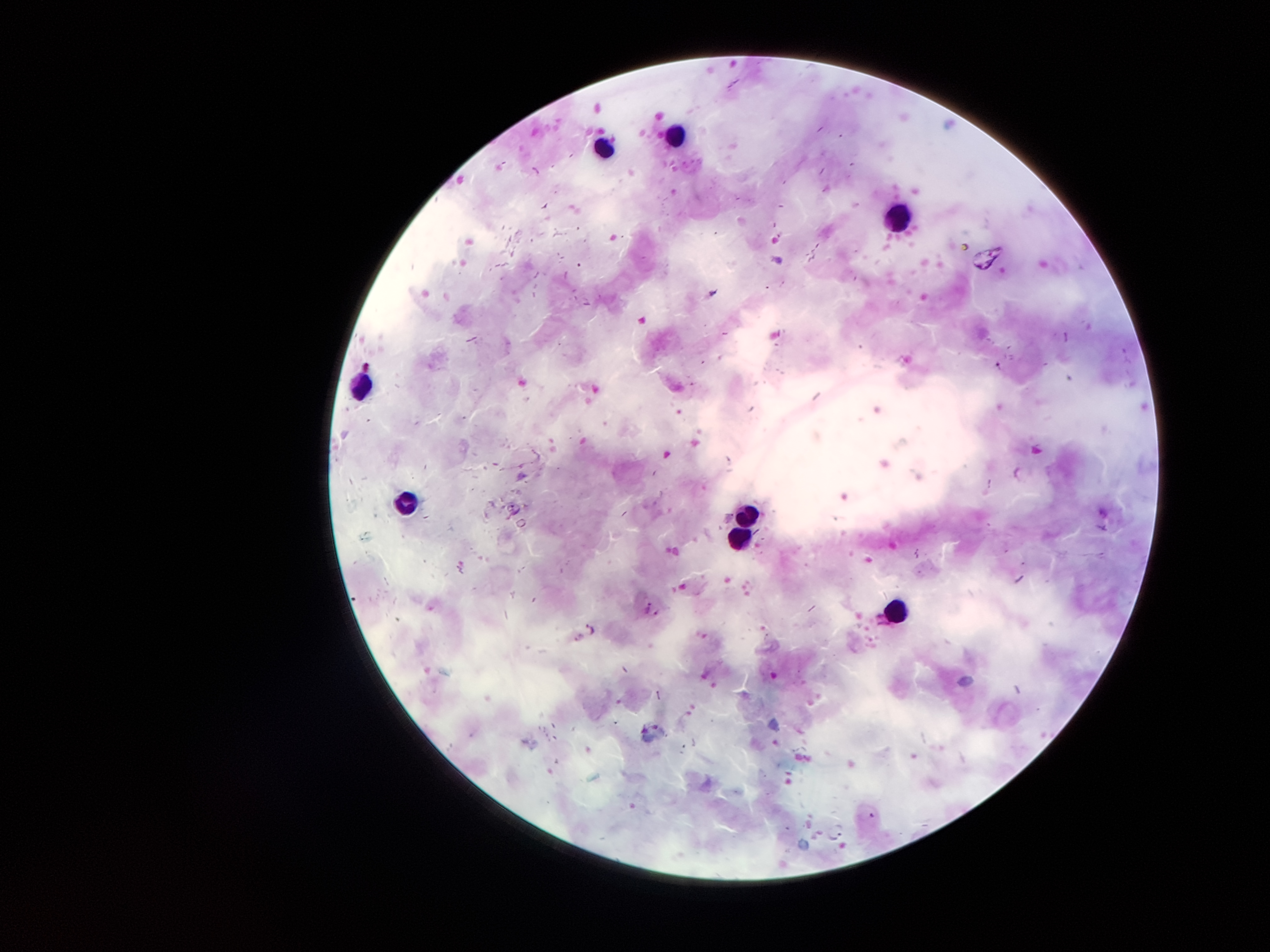
Approximate centers as (x, y) in pixels. Malaria parasite locations: (648, 606), (592, 629). Leukocyte locations: (677, 136), (604, 146), (901, 215), (358, 385), (405, 499), (747, 511), (736, 539), (898, 612). Image is 1270×952 pixels. 100x magnification. Smartphone photograph taken through the microscope eyepiece. One field from this slide. Patient malaria status: infected with Plasmodium falciparum. Giemsa stain. Thick blood smear.